Describe the morphology of the erythrocytes.
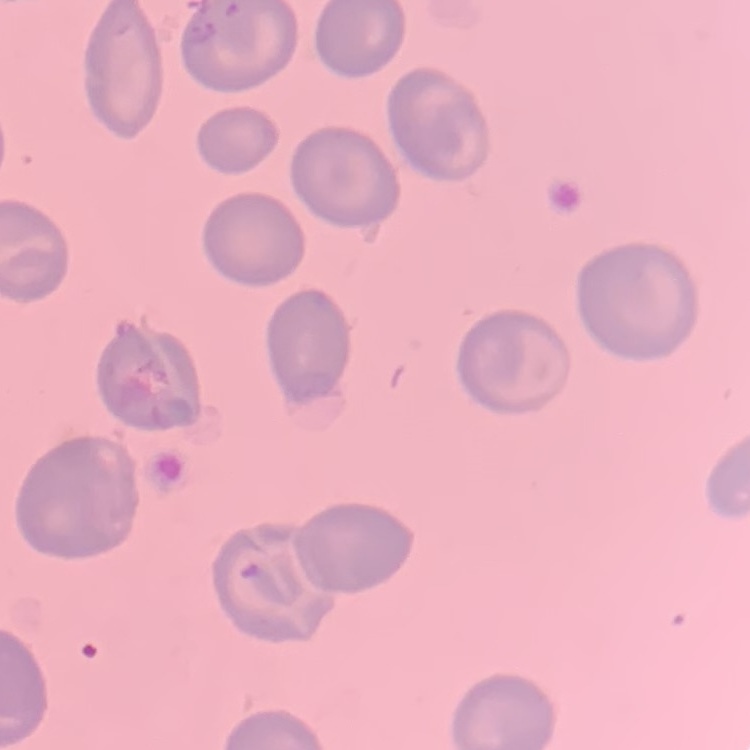

No rouleaux formation.

stain = Field's or Giemsa
preparation = thin blood film
image type = square crop of a larger photomicrograph